Assess the morphology of the erythrocytes.
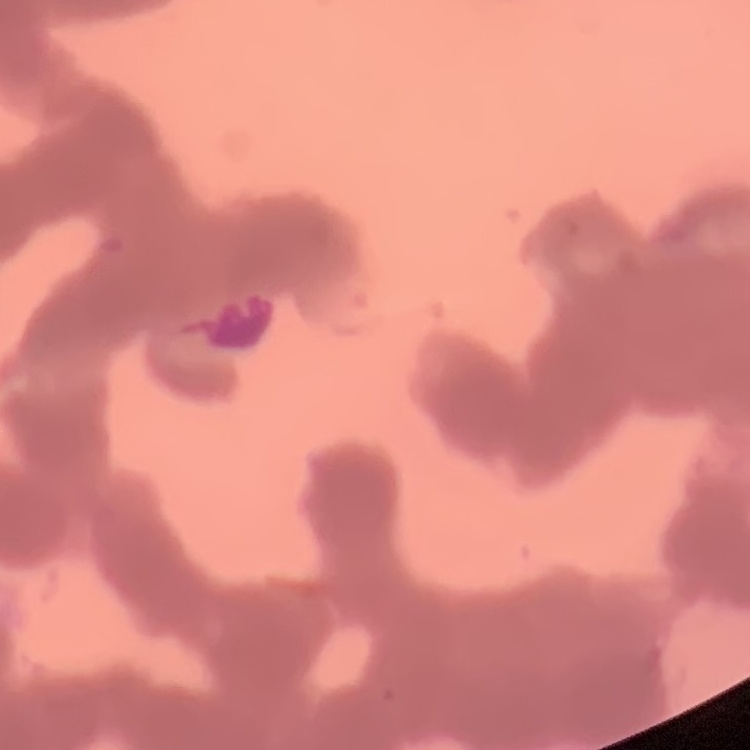

They show rouleaux formation.

preparation: thin blood film
image_type: square crop of a larger photomicrograph
stain: Field's or Giemsa